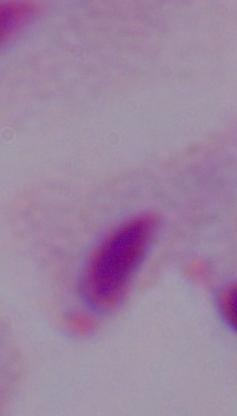
Summary:
  - Modality: micrograph
  - Identification: trichomonad
  - Magnification: 1000x